Locate and identify every blood parasite.
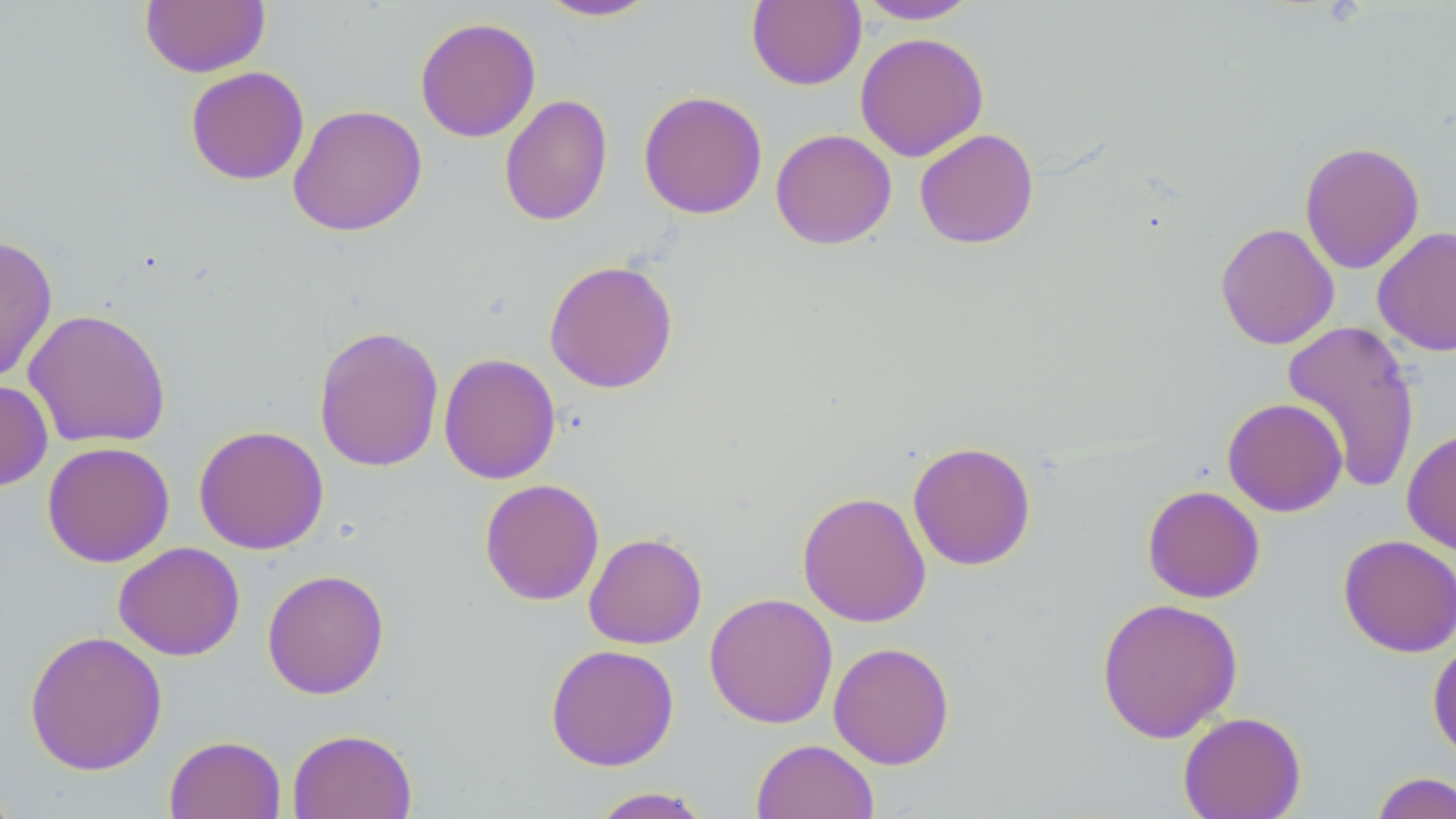
No blood parasites observed.

{
  "slide_level_diagnosis": "negative for blood parasites",
  "field_of_view": "single",
  "modality": "light microscopy",
  "image_size": "1456×819 pixels",
  "preparation": "thin blood film",
  "magnification": "1000x",
  "stain": "May-Grünwald-Giemsa",
  "uninfected_red_blood_cell_locations": "approximate bounding boxes as [x1, y1, x2, y2] in pixels: [139, 1, 270, 78], [536, 1, 661, 22], [746, 1, 866, 90], [856, 1, 980, 24], [414, 16, 541, 143], [855, 32, 989, 162], [185, 66, 310, 186], [638, 90, 768, 219], [498, 93, 613, 227], [287, 103, 427, 236], [770, 128, 897, 249], [914, 128, 1039, 249], [1298, 141, 1425, 275], [1215, 222, 1340, 350], [1372, 226, 1456, 356], [0, 234, 58, 384], [543, 259, 679, 394], [22, 308, 172, 448], [1281, 319, 1421, 494], [313, 324, 444, 472], [438, 353, 561, 485], [0, 379, 53, 492], [1222, 397, 1348, 516], [193, 425, 329, 555], [1402, 427, 1456, 556], [41, 441, 175, 567], [907, 441, 1036, 571], [479, 478, 604, 606], [1142, 484, 1265, 603], [797, 490, 931, 628], [583, 532, 707, 649], [1337, 535, 1456, 657], [113, 542, 246, 661], [262, 568, 389, 699], [704, 592, 838, 728], [1096, 596, 1243, 744], [23, 630, 167, 776], [1427, 636, 1456, 763], [828, 641, 955, 769], [545, 643, 680, 771], [1177, 711, 1307, 819], [288, 728, 417, 818], [164, 734, 286, 819], [751, 739, 880, 819], [0, 770, 19, 819], [1369, 771, 1456, 819], [586, 787, 716, 818]"
}